Assess the morphology of the red blood cells.
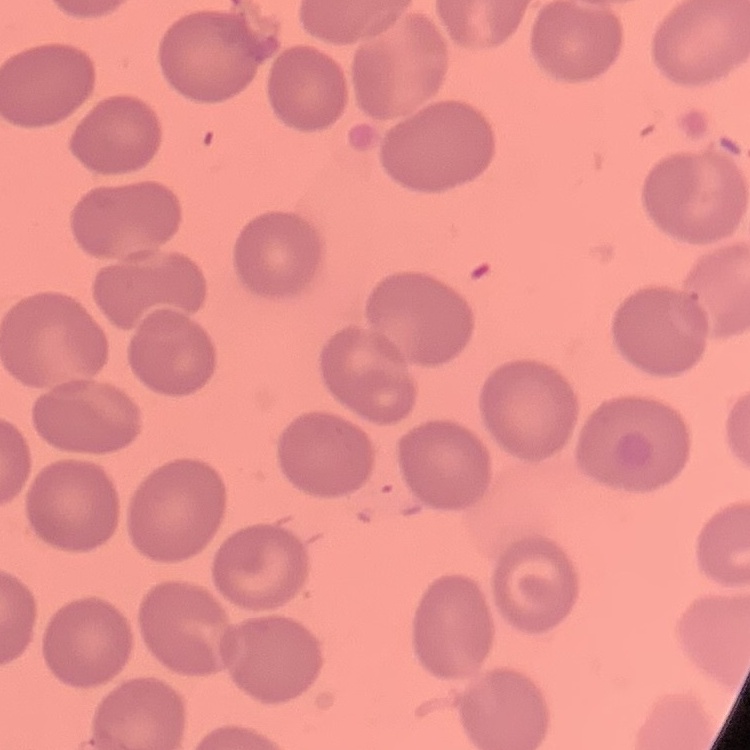

No rouleaux formation.

Thin blood film. One tile cut from a larger photomicrograph. Stained with either Field's or Giemsa.